Assess the morphology of the erythrocytes.
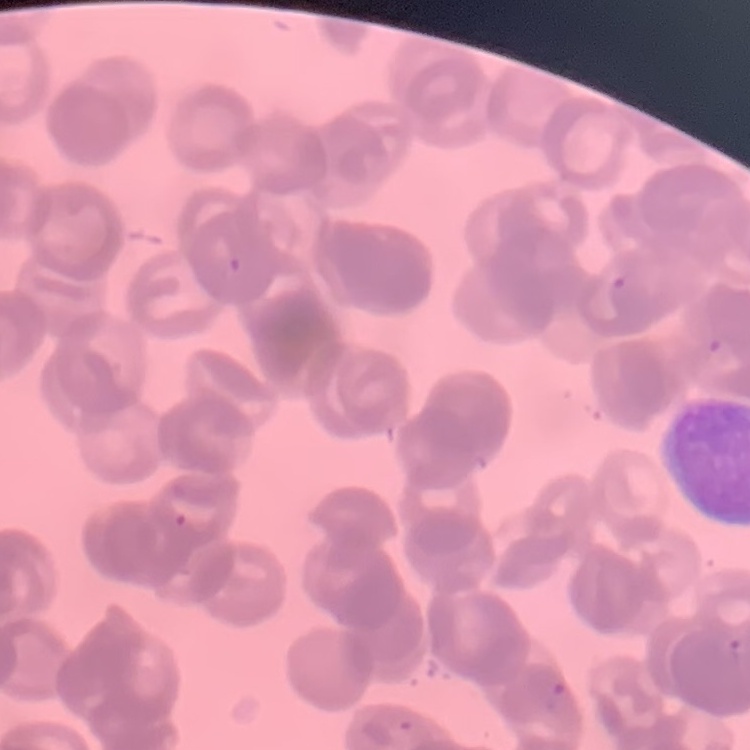

They show rouleaux formation.

Square crop of a larger photomicrograph. Thin peripheral smear. Stained with either Field's or Giemsa.